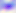

Summary:
  - Magnification: 400x
  - Identification: Toxoplasma gondii
  - Modality: photomicrograph